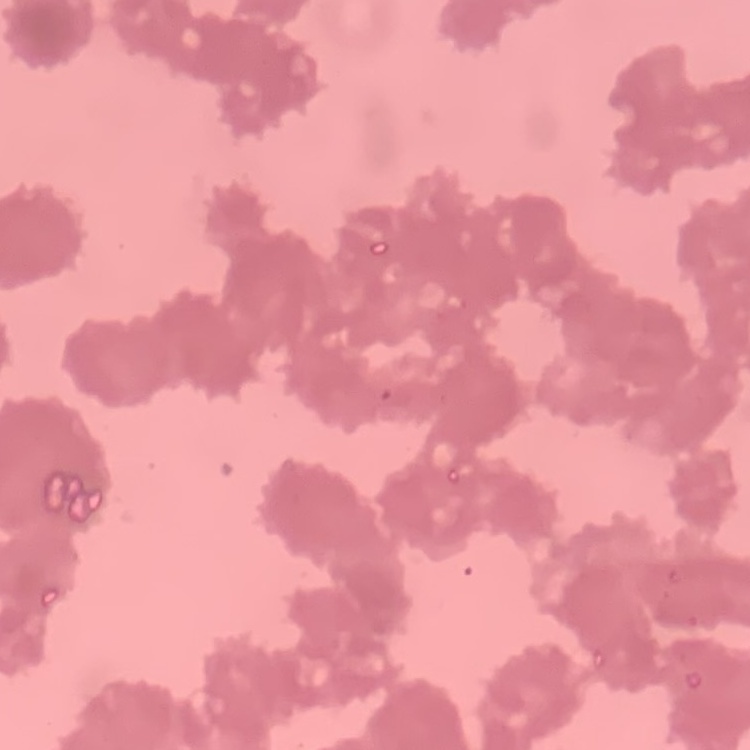
The erythrocytes show rouleaux formation. Field's or Giemsa stain. One tile cut from a larger photomicrograph. Thin peripheral smear.